Assess this cell for malaria.
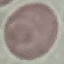
It is uninfected.

Cell patch, automatically extracted from a larger field of view and resized to 64 × 64 pixels. Photographed with a smartphone camera at the microscope eyepiece. Giemsa-stained preparation. Thin blood film.